Outline each blood parasite and name the species.
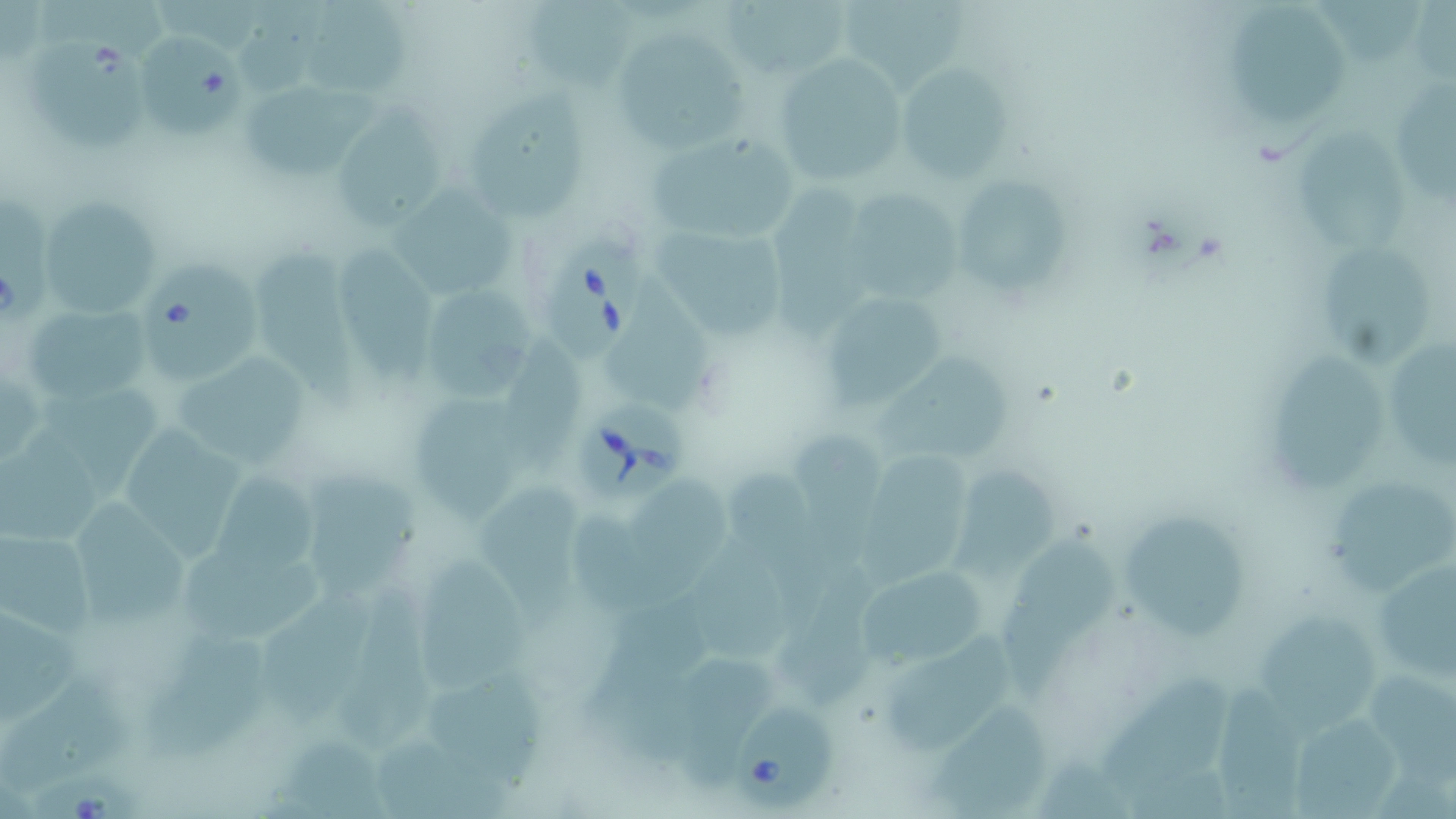
Approximate bounding boxes as (x1, y1, x2, y2) in pixels.
Babesia divergens-infected red blood cells: (544, 241, 639, 359), (579, 400, 690, 502), (729, 698, 835, 809), (28, 771, 142, 819).
No Plasmodium falciparum, Plasmodium ovale, Plasmodium malariae, Plasmodium vivax, or Trypanosoma brucei observed.

slide-level diagnosis = Babesia divergens
modality = optical microscopy
uninfected red blood cell locations = approximate bounding boxes as (x1, y1, x2, y2) in pixels: (718, 0, 855, 77), (303, 1, 417, 99), (514, 1, 635, 92), (840, 1, 968, 87), (232, 3, 339, 90), (137, 27, 252, 136), (613, 30, 744, 153), (1227, 34, 1347, 128), (26, 36, 153, 151), (772, 54, 910, 193), (895, 62, 1015, 185), (462, 78, 592, 223), (1398, 78, 1456, 213), (243, 81, 377, 174), (331, 109, 445, 230), (645, 129, 797, 246), (1292, 133, 1415, 257), (951, 177, 1067, 294), (394, 181, 517, 302), (771, 186, 879, 341), (842, 188, 959, 305), (37, 197, 161, 319), (645, 226, 792, 341), (252, 243, 367, 414), (338, 243, 432, 388), (1311, 243, 1432, 369), (144, 262, 264, 383), (610, 279, 714, 416), (418, 284, 540, 399), (812, 289, 955, 414), (22, 301, 155, 406), (505, 333, 588, 482), (1385, 338, 1456, 478), (1262, 343, 1384, 495), (169, 346, 319, 474), (873, 346, 1018, 467), (37, 381, 164, 507), (409, 389, 521, 526), (120, 420, 243, 565), (0, 428, 116, 543), (791, 428, 883, 560), (860, 451, 975, 584), (951, 457, 1063, 589), (718, 460, 823, 629), (209, 462, 317, 583), (309, 465, 420, 603), (480, 476, 590, 633), (630, 479, 736, 598), (1331, 481, 1456, 600), (72, 495, 190, 623), (1114, 505, 1259, 642), (570, 507, 664, 618), (994, 526, 1117, 699), (0, 528, 94, 639), (692, 530, 796, 669), (1365, 550, 1456, 688), (177, 551, 324, 640), (415, 556, 533, 693), (782, 559, 887, 709), (856, 565, 991, 665), (342, 584, 439, 744), (266, 592, 372, 722), (580, 603, 704, 780), (1259, 603, 1379, 732), (0, 604, 81, 728), (143, 625, 272, 762), (885, 632, 1009, 750), (676, 656, 777, 791), (1097, 666, 1232, 798), (1374, 668, 1456, 788), (423, 670, 551, 795), (1216, 675, 1306, 819), (1, 685, 130, 795), (928, 698, 1052, 818), (1296, 709, 1403, 818), (278, 727, 396, 817), (376, 732, 512, 819), (1041, 750, 1135, 817)
magnification = 1000x
field of view = one of a larger specimen
stain = May-Grünwald-Giemsa
image size = 1456×819 pixels
preparation = thin blood film